Name the cell type shown.
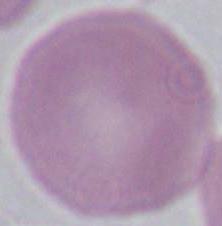
This is an erythrocyte.

1000x magnification. Micrograph.